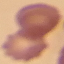

result = no malaria parasites seen
stain = Giemsa
capture = smartphone through the microscope eyepiece
preparation = thin blood film
image type = cell patch, automatically extracted from a larger field of view and resized to 64 × 64 pixels